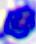
Summary:
  - Magnification: 400x
  - Modality: micrograph
  - Identification: leukocyte